Locate every leukocyte (white blood cell).
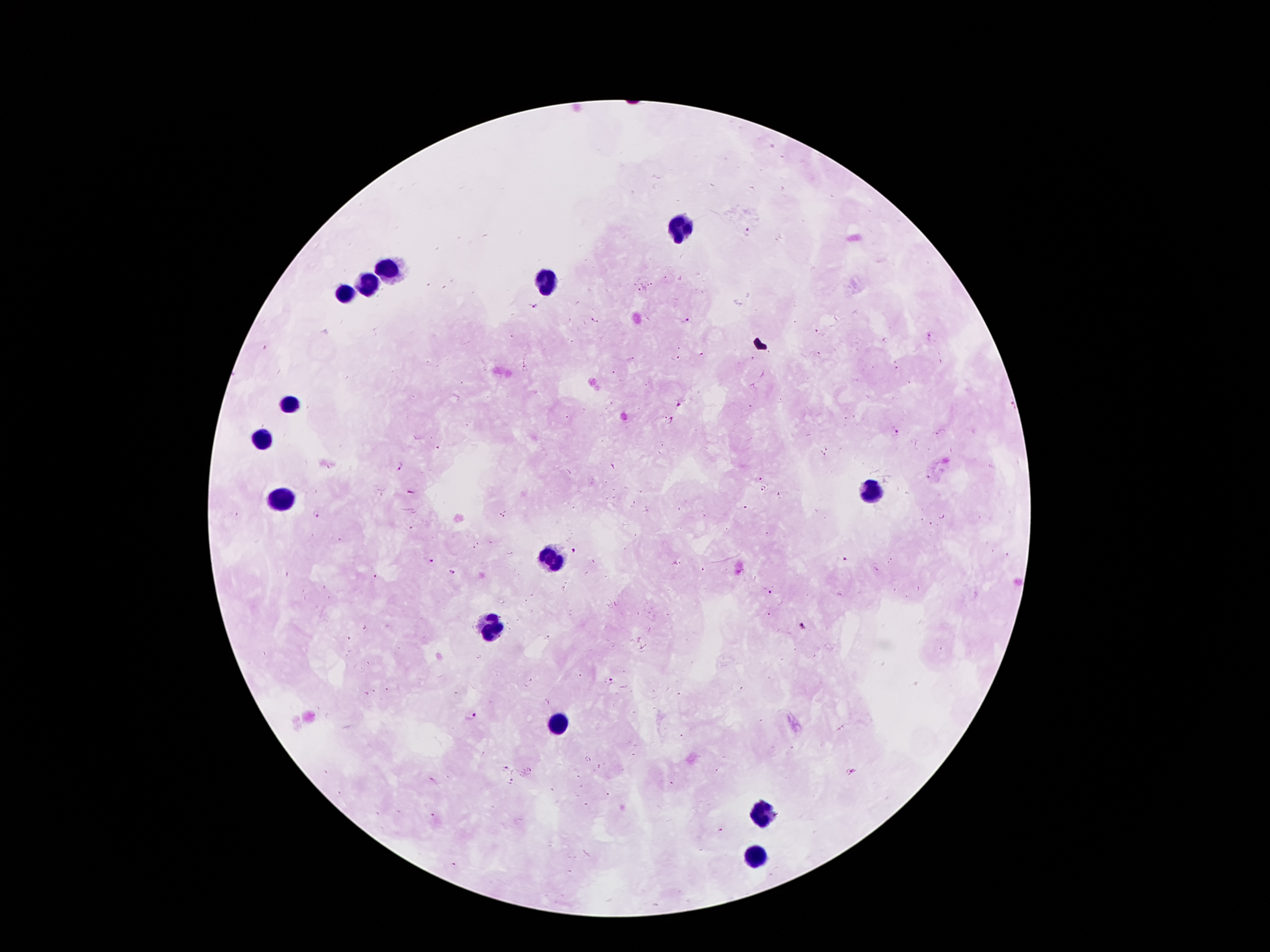

Approximate object centers, in pixels from the top-left corner.
Leukocytes: (x=678, y=225), (x=392, y=268), (x=551, y=277), (x=365, y=284), (x=347, y=293), (x=290, y=404), (x=260, y=438), (x=867, y=493), (x=283, y=502), (x=553, y=554), (x=492, y=629), (x=558, y=726), (x=765, y=817), (x=753, y=856).

Plasmodium parasite locations = (x=746, y=232), (x=536, y=307), (x=685, y=320), (x=596, y=321), (x=930, y=337), (x=702, y=354), (x=676, y=359), (x=631, y=360), (x=896, y=369), (x=524, y=371), (x=613, y=373), (x=680, y=405), (x=664, y=417), (x=672, y=420), (x=895, y=433), (x=942, y=434), (x=829, y=448), (x=821, y=454), (x=399, y=465), (x=763, y=489), (x=317, y=514), (x=503, y=515), (x=942, y=517), (x=574, y=551), (x=430, y=560), (x=845, y=560), (x=876, y=570), (x=453, y=572), (x=375, y=577), (x=770, y=591), (x=803, y=627), (x=548, y=637), (x=580, y=676), (x=610, y=680), (x=532, y=681), (x=475, y=716), (x=505, y=768), (x=531, y=769), (x=512, y=781), (x=720, y=830), (x=453, y=866)
capture = smartphone through the microscope eyepiece
magnification = 100x
image size = 1270×952 pixels
preparation = thick blood film
patient malaria status = positive for Plasmodium falciparum
stain = Giemsa
field of view = single